Comment on the morphology of the erythrocytes.
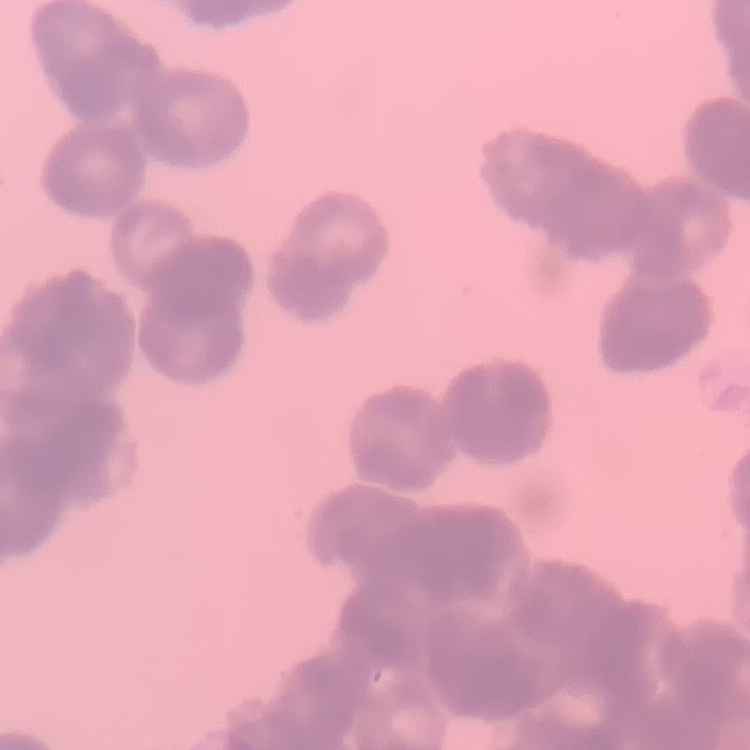
Rouleaux formation.

image type = square crop of a larger photomicrograph
preparation = thin blood smear
stain = Field's or Giemsa